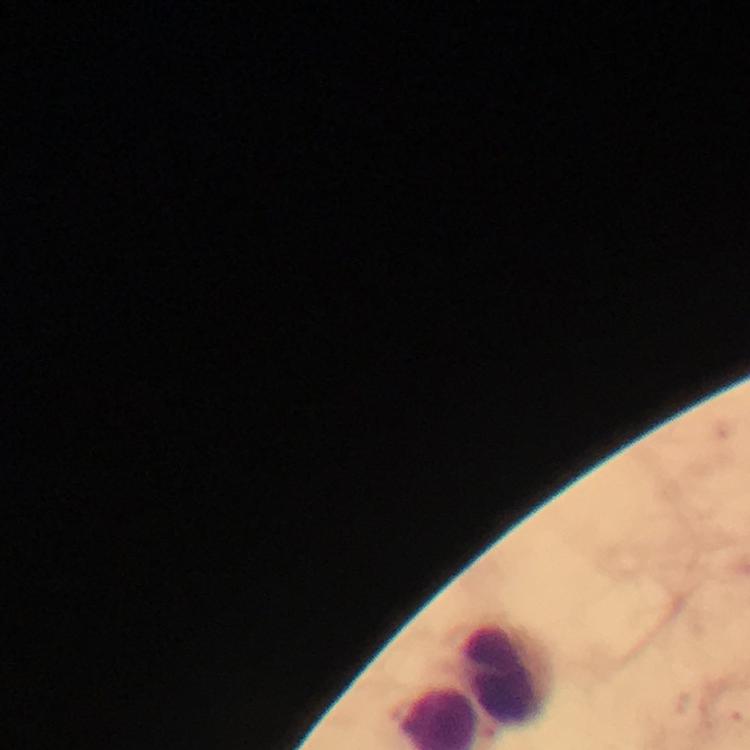

magnification = 100x
leukocyte locations = approximate centers as (x, y) in pixels: (504, 676)
stain = Giemsa
immersion oil = used
image size = 750×750 pixels
Plasmodium parasites = none detected
preparation = thick blood film
context = from a malaria diagnostic workup
capture = smartphone photograph through a microscope
cropped from = a single field of view